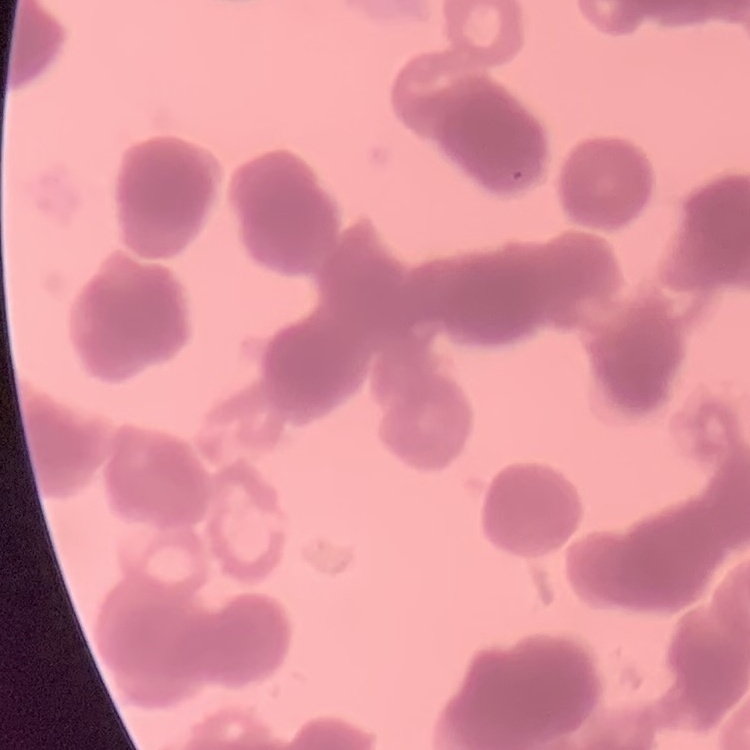
Summary:
  - Erythrocyte morphology: rouleaux formation
  - Image type: square crop of a larger photomicrograph
  - Stain: Field's or Giemsa
  - Preparation: thin peripheral smear